Name the parasite shown.
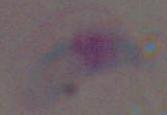

This is Toxoplasma gondii.

magnification = 1000x
modality = micrograph